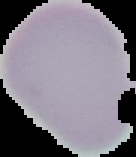 Result: no Plasmodium parasites detected. Cell region segmented out of the field of view; the surrounding area is masked to black. From a thin blood smear. Image is 136×157 pixels.